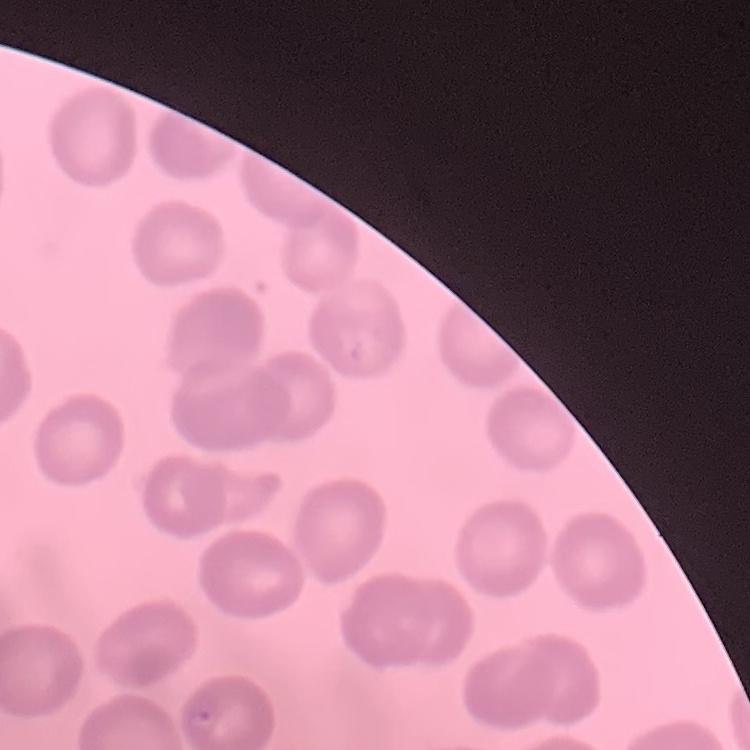

erythrocyte morphology = no rouleaux formation
stain = Field's or Giemsa
image type = square crop of a larger photomicrograph
preparation = thin blood film